Classify this cell by malaria status.
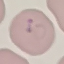
It is parasitized.

preparation = thin blood film
image type = cell patch, automatically extracted from a larger field of view and resized to 64 × 64 pixels
capture = smartphone camera at the microscope eyepiece
stain = Giemsa